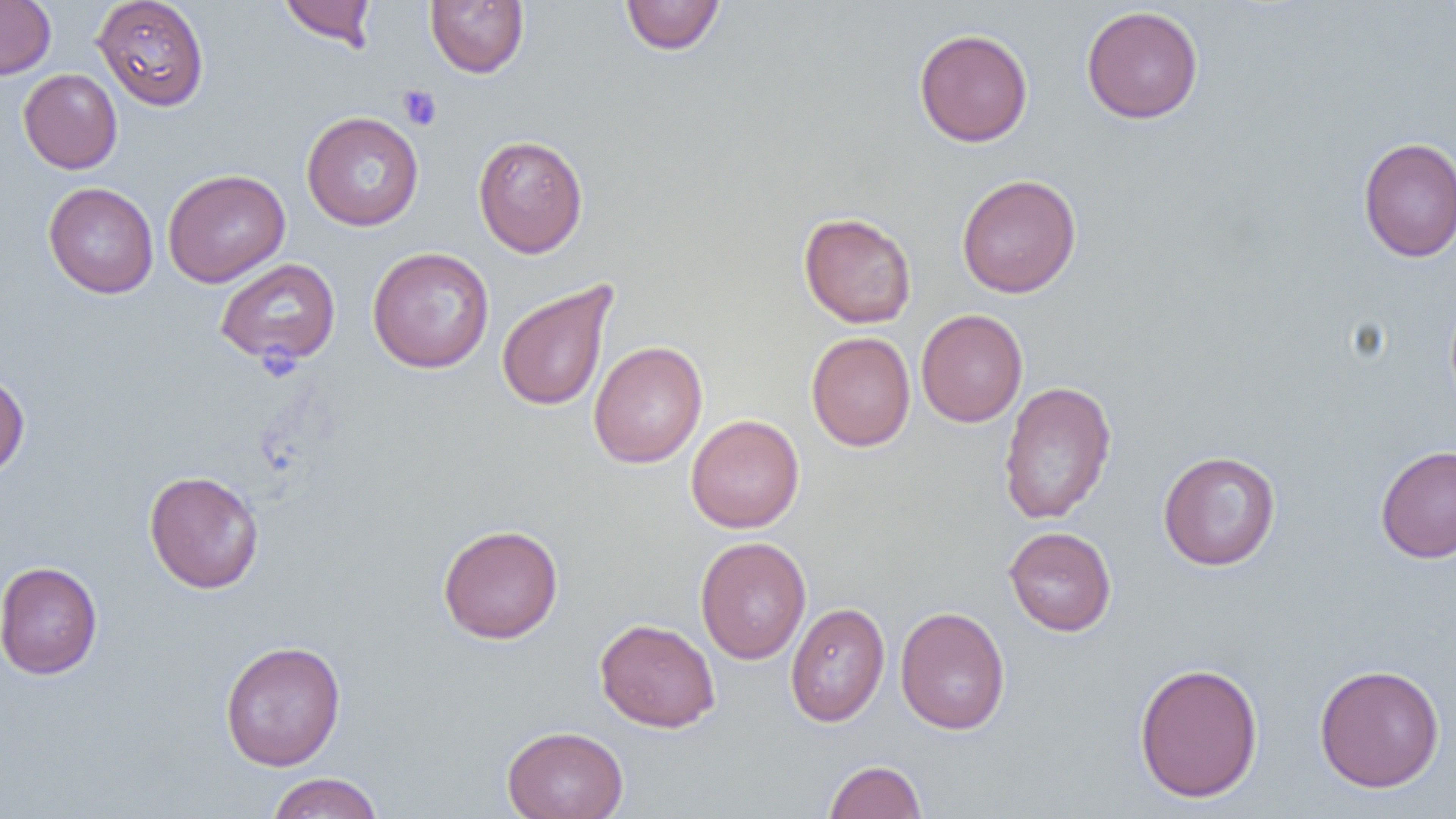

Approximate bounding boxes as [x1, y1, x2, y2] in pixels. Platelet locations: [397, 85, 442, 131]. Uninfected red blood cell locations: [0, 0, 56, 79], [92, 0, 210, 110], [277, 0, 377, 50], [620, 0, 726, 55], [425, 1, 529, 78], [1081, 5, 1204, 124], [914, 28, 1033, 147], [18, 68, 122, 174], [302, 111, 424, 231], [473, 134, 588, 257], [1358, 136, 1456, 262], [162, 169, 290, 288], [957, 173, 1082, 298], [43, 182, 159, 298], [798, 212, 917, 328], [367, 247, 495, 373], [214, 257, 341, 366], [495, 279, 617, 413], [916, 309, 1028, 427], [806, 331, 916, 451], [589, 340, 708, 468], [0, 371, 30, 479], [997, 380, 1117, 524], [685, 414, 804, 533], [1376, 445, 1456, 564], [1158, 450, 1281, 571], [144, 470, 264, 594], [438, 523, 563, 644], [1003, 526, 1117, 636], [695, 536, 812, 664], [0, 561, 102, 679], [786, 602, 890, 727], [895, 606, 1011, 735], [595, 617, 720, 733], [219, 640, 346, 770], [1133, 661, 1263, 802], [1314, 663, 1445, 793], [502, 725, 629, 819], [823, 759, 927, 819], [265, 772, 384, 818]. Slide-level diagnosis: negative for blood parasites. Optical microscopy. Thin blood film. Captured at 1000x magnification. One field of a larger specimen. Image is 1456×819 pixels.